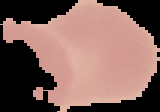

preparation = thin blood film
image size = 160×112 pixels
result = negative for Plasmodium parasites
image type = cell region segmented out of the field of view; surrounding area masked to black